Classify this cell by malaria status.
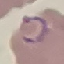
Parasitized.

Acquired by smartphone through the microscope eyepiece. Thin blood smear. Automatically extracted cell patch, resized to 64 × 64 pixels. Giemsa stain.